Locate every blood parasite and identify its species.
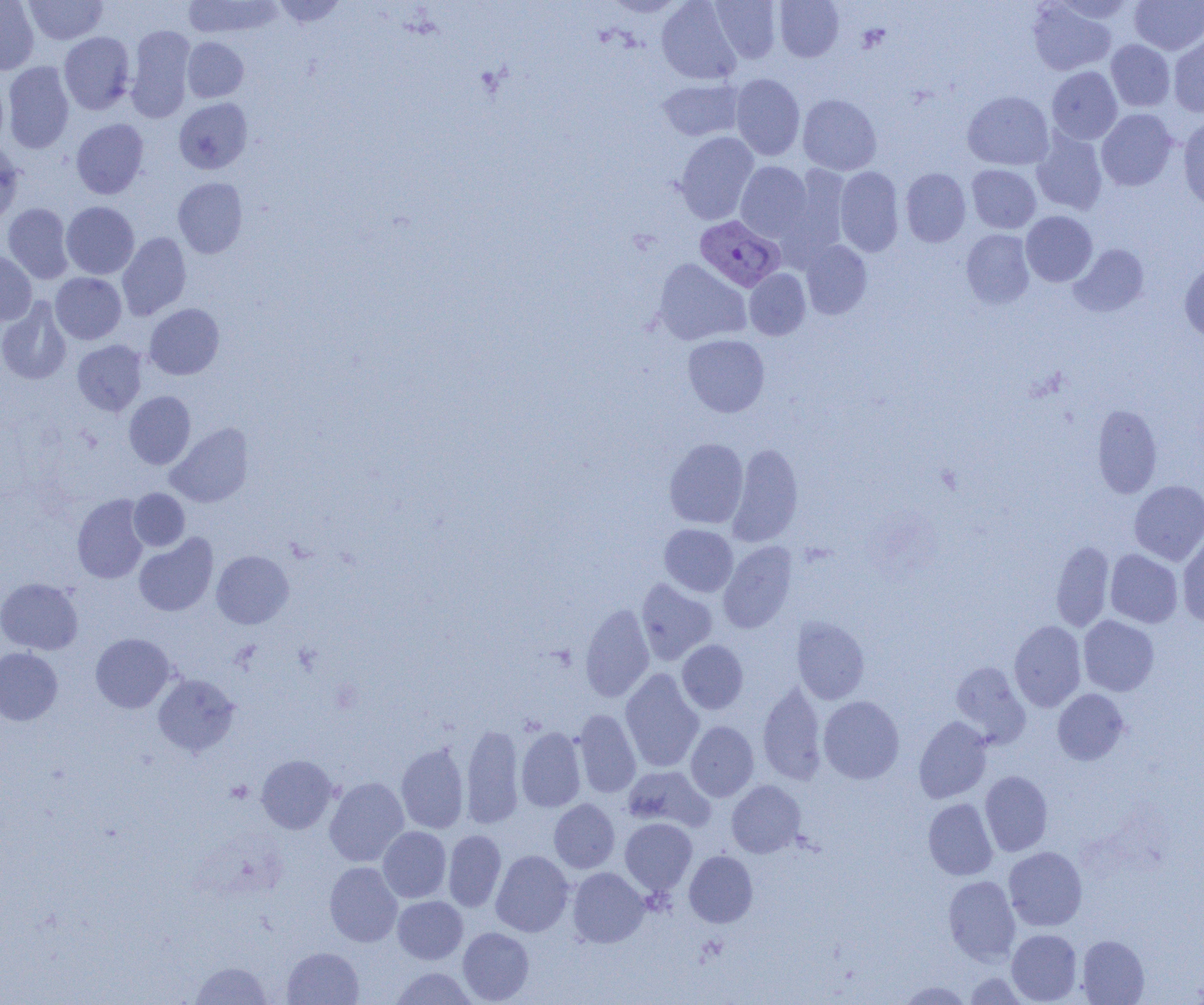
Approximate bounding boxes as (x1,y1)-(x2,y2) corner pairs in pixels.
Plasmodium vivax-infected red blood cells: (695,216)-(785,292).
No Plasmodium falciparum, Plasmodium ovale, Plasmodium malariae, Babesia divergens, or Trypanosoma brucei observed.

Summary:
  - Platelet locations: (225,780)-(252,804)
  - Uninfected red blood cell locations: (24,0)-(107,45), (183,0)-(283,40), (271,0)-(347,28), (601,0)-(687,17), (657,0)-(742,85), (710,0)-(782,63), (775,0)-(844,61), (1050,0)-(1138,24), (1130,0)-(1204,54), (0,1)-(39,74), (1027,1)-(1116,75), (125,25)-(195,122), (59,32)-(135,114), (1169,34)-(1204,117), (182,37)-(249,102), (1106,40)-(1175,112), (3,62)-(74,153), (1047,66)-(1122,144), (731,73)-(804,160), (0,75)-(8,151), (657,78)-(744,141), (963,91)-(1054,170), (797,94)-(882,175), (174,98)-(252,174), (1096,108)-(1177,191), (1178,114)-(1204,210), (71,119)-(149,199), (1031,131)-(1107,215), (675,132)-(758,224), (0,141)-(24,226), (736,161)-(813,241), (778,165)-(851,266), (967,165)-(1041,233), (835,166)-(904,257), (901,168)-(970,247), (173,177)-(248,258), (61,202)-(139,279), (2,203)-(74,284), (1021,211)-(1097,287), (961,229)-(1034,308), (117,232)-(191,320), (801,240)-(872,319), (1069,244)-(1150,317), (0,251)-(37,325), (653,258)-(751,346), (1179,261)-(1204,343), (744,269)-(810,340), (51,273)-(126,344), (0,297)-(71,385), (145,304)-(224,379), (683,334)-(770,417), (72,340)-(147,416), (124,391)-(196,469), (1092,405)-(1162,497), (165,422)-(253,507), (664,437)-(748,529), (727,442)-(803,546), (1129,480)-(1204,565), (129,488)-(190,551), (72,494)-(149,583), (659,524)-(738,597), (1177,533)-(1204,627), (134,534)-(218,617), (718,541)-(797,633), (1051,541)-(1114,631), (1105,549)-(1183,628), (211,550)-(294,629), (0,578)-(83,655), (636,578)-(717,665), (580,603)-(654,702), (1078,615)-(1159,696), (791,617)-(870,704), (1009,620)-(1086,712), (90,633)-(176,713), (677,639)-(748,714), (0,647)-(63,725), (950,661)-(1031,747), (620,669)-(704,772), (152,674)-(240,757), (758,681)-(827,784), (1053,689)-(1129,765), (818,696)-(904,784), (573,708)-(641,798), (914,716)-(992,803), (685,721)-(759,802), (460,724)-(525,828), (516,727)-(586,812), (396,743)-(469,833), (256,754)-(338,834), (622,765)-(715,832), (980,771)-(1053,856), (324,776)-(409,867), (726,780)-(805,857), (549,798)-(620,873), (923,798)-(998,880), (620,818)-(697,895), (378,827)-(451,902), (443,830)-(506,911), (1004,846)-(1087,930), (491,850)-(574,937), (684,850)-(757,927), (324,861)-(403,946), (567,867)-(649,947), (943,875)-(1020,965), (392,896)-(468,964), (458,927)-(534,1003), (1006,929)-(1083,1004), (1076,934)-(1149,1004), (282,947)-(363,1005), (190,961)-(272,1004), (389,967)-(479,1004), (964,972)-(1031,1005), (896,980)-(973,1004)
  - Slide-level diagnosis: Plasmodium vivax
  - Preparation: thin blood film
  - Field of view: one of a larger specimen
  - Magnification: 1000x
  - Modality: light microscopy
  - Image size: 1204×1005 pixels